Report the malaria status of this cell.
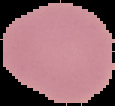
Uninfected.

image_type: segmented cell region on a black background
preparation: thin blood film
image_size: 115×106 pixels